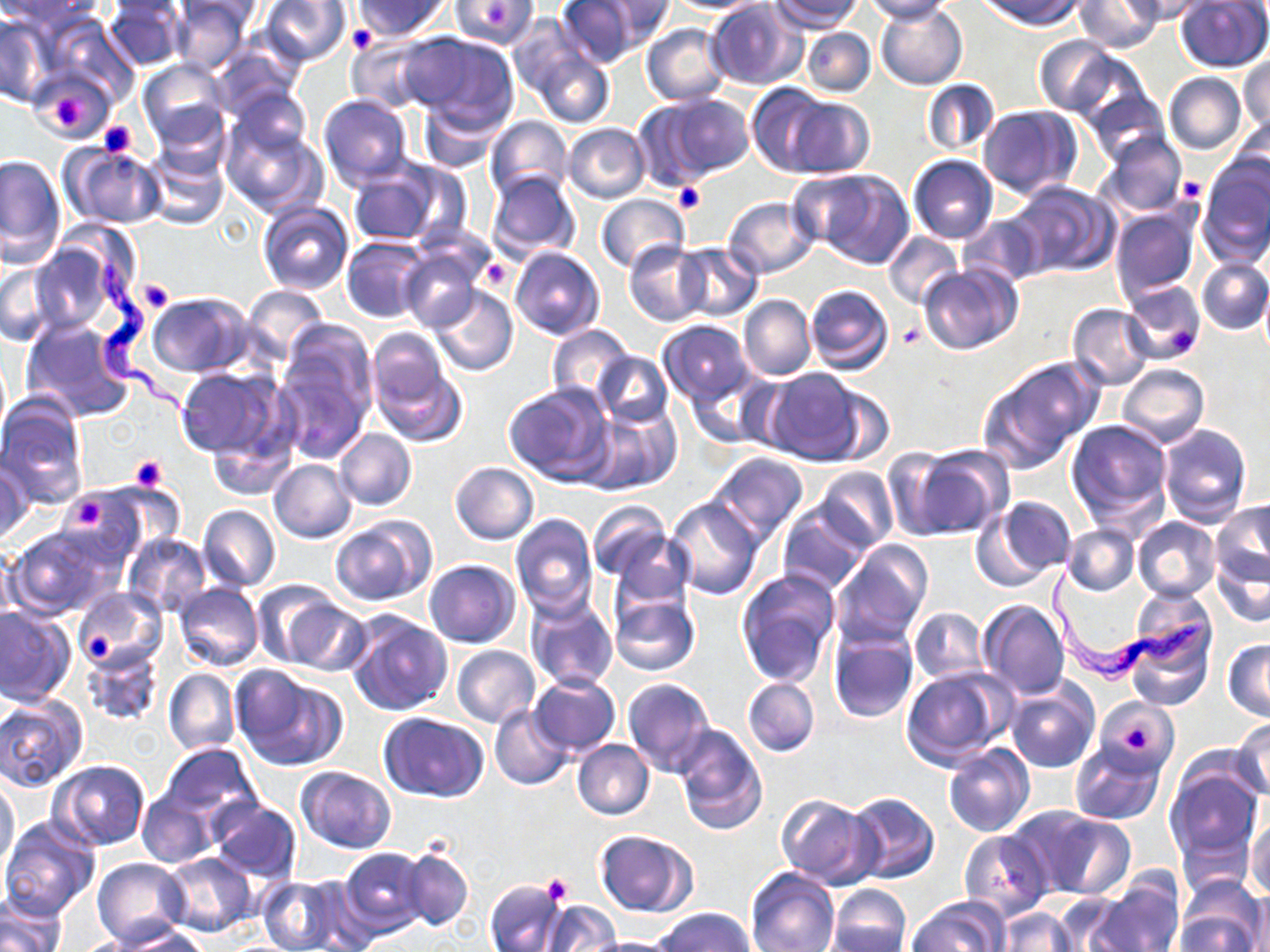

slide-level diagnosis = Trypanosoma brucei
platelet locations = approximate bounding boxes as (x1, y1, x2, y2) in pixels: (346, 23, 376, 52), (55, 96, 87, 128), (97, 120, 136, 161), (1177, 176, 1207, 202), (673, 183, 705, 215), (479, 256, 513, 290), (138, 279, 172, 312), (896, 323, 923, 349), (1172, 326, 1201, 353), (129, 454, 166, 492), (61, 490, 114, 538), (81, 626, 119, 665), (1123, 724, 1153, 755), (541, 874, 575, 908)
Trypanosoma brucei locations = approximate bounding boxes as (x1, y1, x2, y2) in pixels: (91, 254, 220, 432), (1044, 562, 1206, 690)
magnification = 1000x
uninfected red blood cell locations = approximate bounding boxes as (x1, y1, x2, y2) in pixels: (102, 0, 186, 70), (169, 0, 257, 74), (259, 0, 352, 67), (352, 0, 450, 41), (556, 0, 638, 69), (596, 0, 675, 46), (659, 0, 771, 13), (705, 0, 808, 89), (768, 0, 865, 33), (862, 0, 956, 23), (981, 0, 1086, 31), (1120, 0, 1210, 23), (5, 1, 103, 32), (176, 1, 263, 29), (450, 1, 539, 46), (1073, 1, 1164, 52), (1177, 1, 1270, 72), (875, 3, 968, 90), (0, 13, 50, 107), (42, 14, 142, 106), (508, 16, 587, 99), (640, 23, 730, 105), (801, 26, 876, 96), (401, 32, 519, 134), (1033, 35, 1127, 118), (346, 36, 437, 113), (209, 44, 301, 119), (532, 50, 614, 129), (1238, 56, 1269, 136), (138, 58, 231, 147), (31, 66, 121, 139), (1164, 72, 1246, 155), (923, 78, 1001, 156), (746, 84, 834, 175), (230, 85, 309, 158), (1082, 87, 1169, 164), (780, 94, 875, 179), (319, 95, 414, 188), (660, 95, 754, 180), (419, 100, 507, 174), (146, 102, 231, 177), (635, 104, 717, 191), (977, 106, 1078, 201), (1227, 113, 1270, 195), (485, 116, 572, 203), (220, 117, 325, 218), (564, 123, 650, 204), (1096, 133, 1187, 217), (61, 145, 166, 229), (140, 146, 230, 232), (1, 154, 65, 263), (909, 154, 998, 244), (1197, 159, 1270, 265), (347, 163, 452, 250), (796, 169, 912, 266), (486, 171, 581, 264), (1010, 182, 1118, 277), (596, 194, 688, 275), (724, 196, 819, 278), (257, 201, 354, 296), (1110, 206, 1200, 301), (959, 214, 1045, 286), (883, 232, 963, 310), (343, 235, 433, 322), (27, 236, 130, 338), (624, 239, 710, 327), (672, 242, 762, 322), (510, 247, 605, 340), (399, 249, 484, 330), (1198, 259, 1270, 334), (0, 261, 57, 346), (918, 265, 1022, 355), (1120, 282, 1206, 367), (241, 283, 329, 363), (1258, 283, 1270, 358), (804, 284, 893, 375), (430, 285, 519, 376), (149, 293, 250, 377), (738, 295, 816, 381), (1068, 303, 1156, 390), (278, 318, 377, 429), (20, 319, 134, 422), (656, 320, 756, 407), (545, 324, 633, 403), (592, 351, 673, 427), (373, 353, 466, 446), (978, 357, 1100, 474), (1119, 364, 1209, 450), (177, 366, 284, 460), (762, 368, 869, 465), (686, 371, 777, 449), (502, 381, 614, 486), (0, 397, 90, 509), (579, 405, 682, 496), (1067, 420, 1172, 525), (1157, 423, 1251, 528), (334, 428, 417, 511), (206, 431, 295, 502), (905, 445, 1012, 540), (705, 451, 809, 543), (269, 459, 357, 544), (0, 460, 33, 546), (450, 461, 539, 545), (813, 466, 898, 551), (988, 496, 1076, 582), (665, 497, 766, 600), (587, 501, 672, 583), (777, 502, 873, 596), (1211, 502, 1270, 590), (197, 504, 280, 591), (510, 514, 599, 617), (1133, 517, 1220, 602), (330, 518, 433, 606), (1063, 524, 1138, 596), (10, 526, 119, 619), (608, 529, 696, 611), (123, 533, 211, 617), (832, 540, 932, 646), (0, 543, 20, 627), (1211, 544, 1269, 628), (424, 559, 520, 648), (737, 568, 842, 687), (253, 580, 343, 668), (173, 582, 263, 672), (73, 588, 164, 669), (1129, 589, 1215, 671), (609, 590, 700, 676), (526, 594, 617, 692), (283, 599, 372, 676), (977, 600, 1069, 700), (0, 606, 75, 706), (910, 607, 988, 684), (347, 612, 452, 716), (1124, 620, 1215, 714), (827, 629, 918, 724), (1223, 639, 1270, 720), (81, 646, 164, 726), (452, 646, 540, 727), (901, 667, 1006, 768), (163, 669, 240, 754), (236, 670, 347, 771), (529, 674, 619, 756), (621, 677, 715, 777), (742, 678, 819, 756), (1005, 680, 1099, 772), (0, 696, 86, 791), (1100, 699, 1179, 771), (490, 706, 575, 790), (378, 712, 489, 802), (1231, 719, 1270, 800), (671, 724, 767, 836), (158, 739, 261, 824), (1070, 739, 1166, 825), (572, 740, 654, 819), (943, 743, 1035, 837), (50, 759, 151, 850), (1163, 764, 1263, 862), (296, 767, 396, 853), (0, 777, 20, 872), (845, 791, 940, 884), (137, 792, 219, 867), (775, 793, 877, 887), (207, 798, 302, 883), (1247, 812, 1270, 899), (1039, 814, 1134, 900), (1, 816, 100, 918), (594, 830, 698, 917), (958, 830, 1054, 922), (338, 847, 430, 936), (399, 847, 472, 931), (161, 852, 256, 938), (92, 857, 188, 947), (745, 867, 839, 952), (1173, 874, 1266, 951), (255, 875, 347, 952), (1088, 877, 1183, 952), (485, 878, 565, 952), (828, 884, 910, 952), (1250, 888, 1270, 952), (0, 893, 66, 952), (1049, 894, 1134, 949), (908, 896, 1007, 952), (541, 899, 620, 951), (996, 907, 1076, 952), (656, 908, 754, 952), (107, 924, 209, 952), (584, 936, 682, 950)
modality = optical microscopy
preparation = thin blood film
stain = May-Grünwald-Giemsa
image size = 1270×952 pixels
field of view = single